Name the parasite shown.
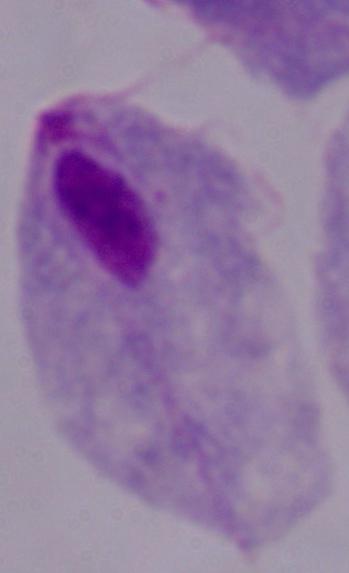
This is a trichomonad.

{
  "modality": "micrograph",
  "magnification": "1000x"
}